Locate the cells, classifying each as a parasitized RBC, an uninfected RBC, or a WBC.
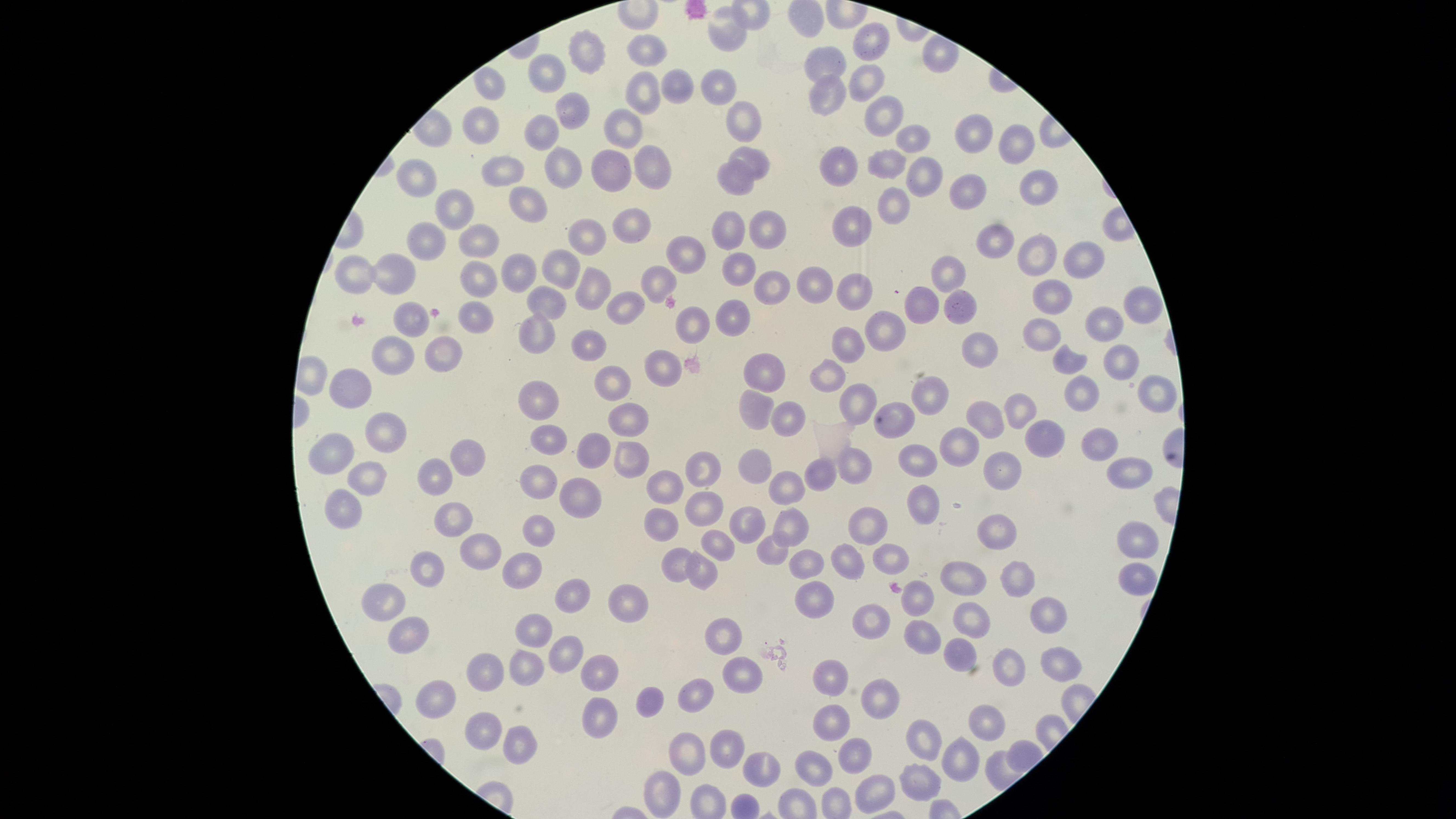
No parasitized RBCs identified.
Approximate marker points as {x, y} in pixels.
Uninfected RBCs: {731, 27}, {871, 47}, {650, 50}, {584, 55}, {827, 64}, {868, 74}, {546, 78}, {680, 80}, {714, 85}, {491, 86}, {825, 91}, {639, 100}, {570, 110}, {884, 110}, {745, 116}, {485, 125}, {623, 128}, {914, 133}, {974, 133}, {544, 134}, {1010, 143}, {752, 162}, {559, 164}, {842, 164}, {645, 165}, {888, 165}, {504, 168}, {920, 171}, {611, 172}, {421, 181}, {735, 181}, {1041, 183}, {970, 200}, {890, 201}, {524, 206}, {461, 207}, {850, 225}, {775, 226}, {635, 228}, {582, 235}, {731, 235}, {427, 241}, {477, 241}, {994, 241}, {688, 251}, {1041, 254}, {1087, 258}, {521, 265}, {559, 267}, {360, 271}, {394, 271}, {740, 271}, {947, 273}, {658, 284}, {774, 285}, {472, 286}, {597, 286}, {859, 287}, {820, 290}, {1055, 294}, {1136, 301}, {548, 302}, {632, 302}, {923, 303}, {961, 305}, {691, 315}, {476, 319}, {416, 320}, {736, 320}, {1105, 325}, {884, 326}, {1043, 332}, {537, 333}, {852, 345}, {592, 346}, {981, 347}, {446, 354}, {397, 357}, {653, 360}, {1124, 361}, {1074, 363}, {772, 370}, {817, 379}, {614, 380}, {355, 385}, {1161, 389}, {538, 393}, {1073, 393}, {934, 402}, {855, 405}, {758, 407}, {1021, 408}, {788, 418}, {889, 419}, {984, 420}, {633, 421}, {389, 426}, {548, 429}, {1042, 433}, {1094, 449}, {955, 451}, {339, 456}, {915, 456}, {584, 457}, {463, 459}, {623, 462}, {753, 464}, {851, 467}, {699, 468}, {1007, 472}, {820, 473}, {374, 477}, {439, 477}, {1120, 478}, {793, 485}, {541, 486}, {663, 491}, {576, 496}, {921, 503}, {699, 506}, {345, 507}, {451, 517}, {748, 523}, {868, 523}, {659, 526}, {790, 531}, {538, 532}, {996, 535}, {1138, 541}, {714, 546}, {480, 547}, {770, 548}, {889, 553}, {673, 556}, {805, 559}, {854, 560}, {523, 565}, {427, 571}, {700, 575}, {960, 576}, {1132, 576}, {1015, 579}, {565, 590}, {811, 595}, {380, 600}, {919, 600}, {626, 605}, {969, 612}, {1049, 614}, {871, 621}, {537, 630}, {408, 633}, {726, 636}, {920, 642}, {564, 651}, {964, 653}, {1057, 661}, {527, 666}, {1013, 668}, {742, 669}, {488, 672}, {594, 672}, {836, 676}, {698, 693}, {886, 694}, {442, 697}, {648, 701}, {594, 719}, {834, 719}, {991, 721}, {483, 724}, {924, 741}, {514, 743}, {721, 747}, {691, 752}, {856, 753}, {963, 758}, {817, 767}, {760, 770}, {914, 777}, {665, 791}, {870, 795}.
No WBCs identified.

Thin blood smear. Circular visible region. Smartphone photograph through the microscope eyepiece. Image is 1456×819 pixels. Single field of view. Giemsa stain.